Outline platelets.
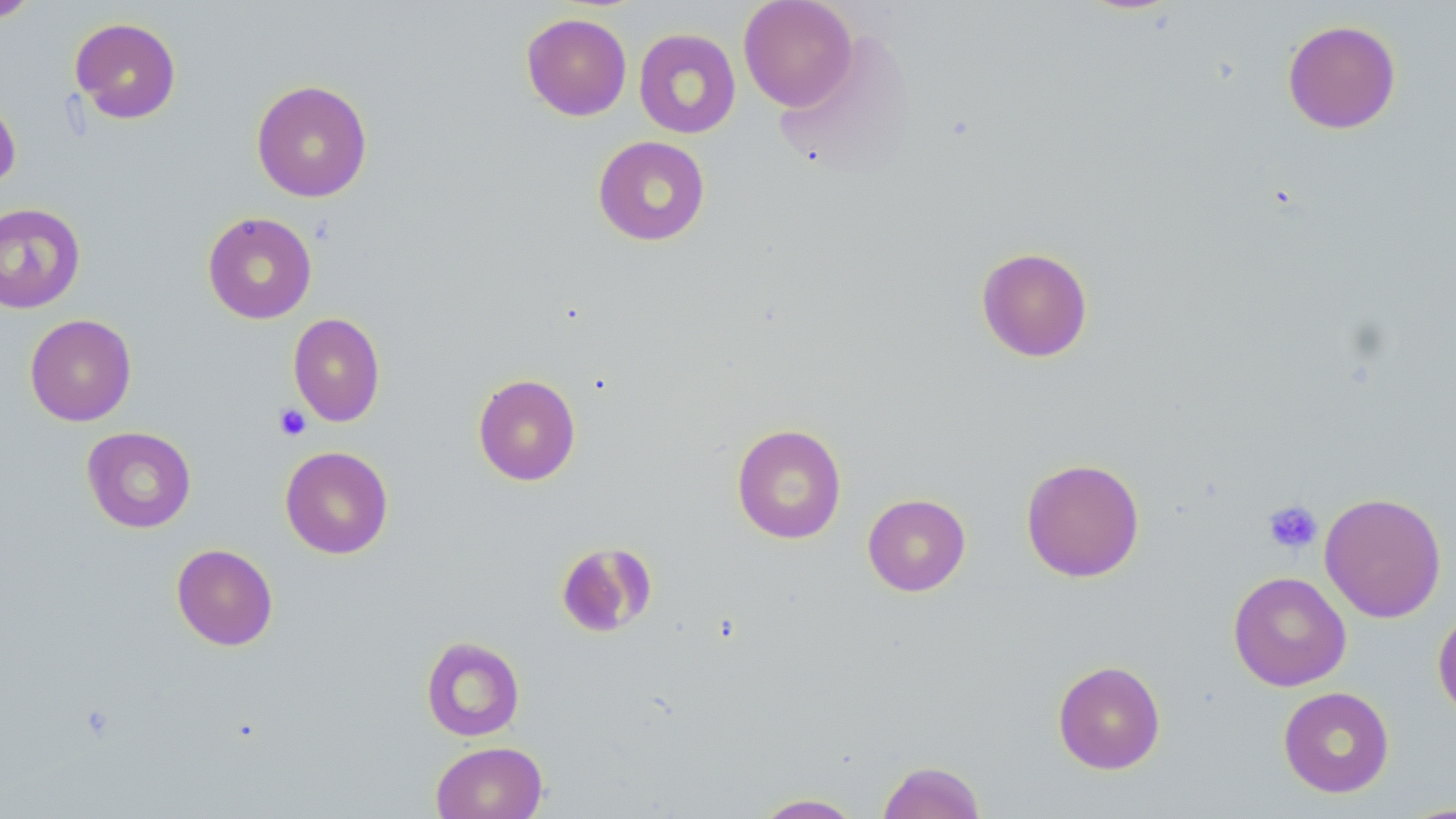
Approximate bounding boxes as (x1,y1)-(x2,y2) corner pairs in pixels.
Platelets: (273,404)-(311,441), (1262,500)-(1323,555).

slide-level diagnosis = no evidence of blood parasites
field of view = single
magnification = 1000x
stain = May-Grünwald-Giemsa
uninfected red blood cell locations = approximate bounding boxes as (x1,y1)-(x2,y2) corner pairs in pixels: (0,0)-(41,24), (738,0)-(857,111), (521,13)-(632,121), (70,17)-(182,124), (1282,19)-(1402,134), (634,28)-(741,139), (251,79)-(373,202), (0,91)-(21,192), (593,135)-(710,246), (0,203)-(86,314), (202,211)-(317,324), (976,247)-(1093,362), (288,312)-(386,427), (24,314)-(137,426), (473,373)-(581,486), (731,423)-(847,544), (82,426)-(196,533), (280,446)-(394,559), (1021,458)-(1145,582), (1319,492)-(1447,623), (862,493)-(971,596), (554,542)-(656,638), (171,543)-(278,650), (1228,571)-(1351,691), (1432,606)-(1456,721), (421,636)-(525,742), (1052,660)-(1166,774), (1278,686)-(1394,797), (430,741)-(548,819), (876,760)-(986,819), (752,793)-(865,818), (1397,802)-(1456,818)
image size = 1456×819 pixels
modality = light microscopy
preparation = thin blood smear